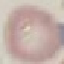
malaria status = uninfected
preparation = thin blood smear
image type = cell patch, automatically extracted from a larger field of view and resized to 64 × 64 pixels
stain = Giemsa
capture = smartphone through the microscope eyepiece